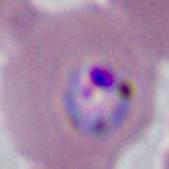 Photomicrograph. A Plasmodium parasite is shown. 400x or 1000x magnification.